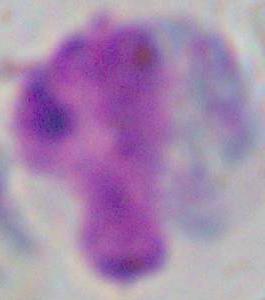

Micrograph. A white blood cell is seen. 1000x magnification.